Identify the preparation type.
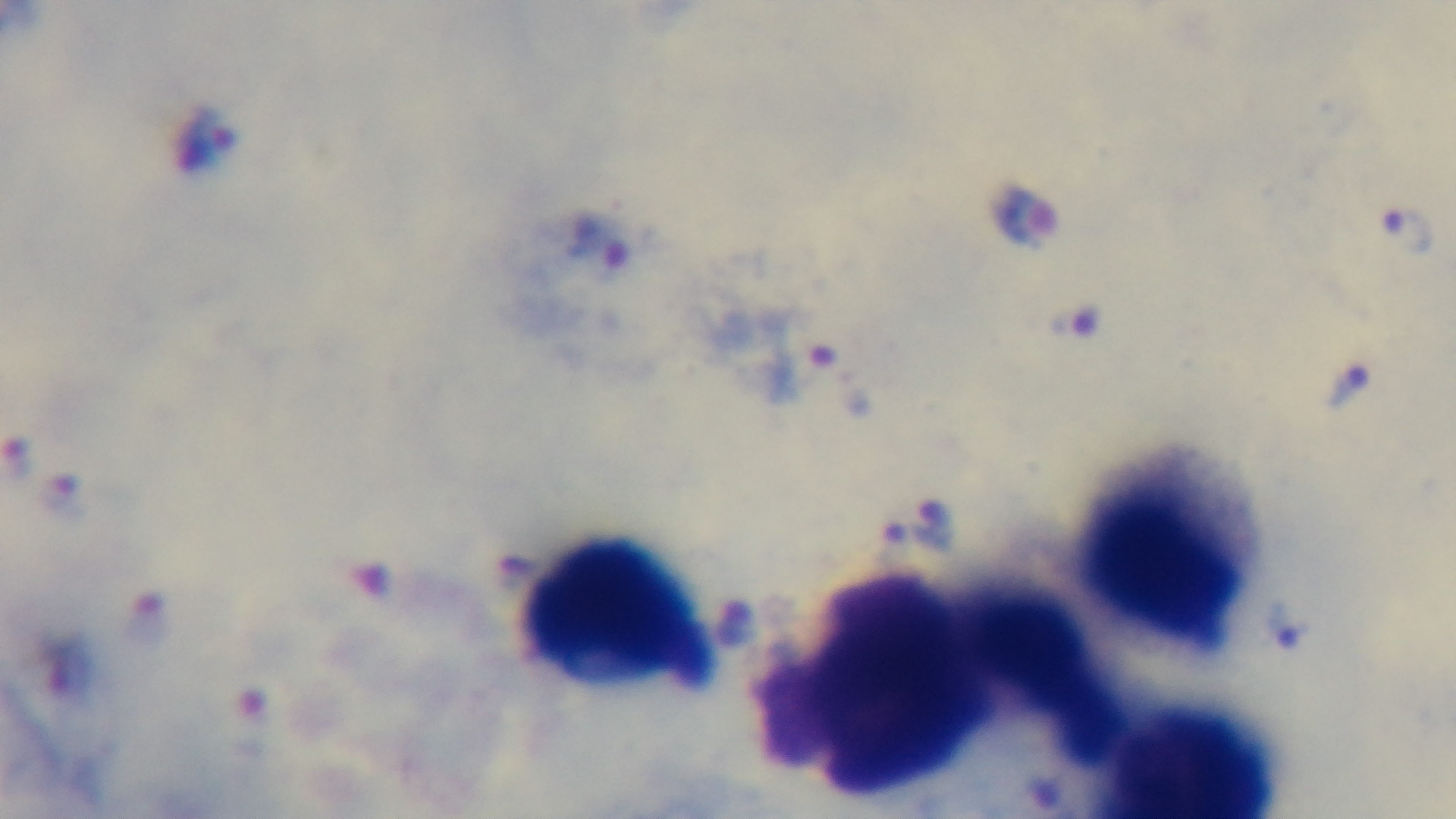

It is a thick blood film.

Photomicrograph. Malaria status: infected. One field from the slide. Giemsa-stained. Mounted 4K digital camera. Oil-immersion objective, 100x.